Comment on the morphology of the red blood cells.
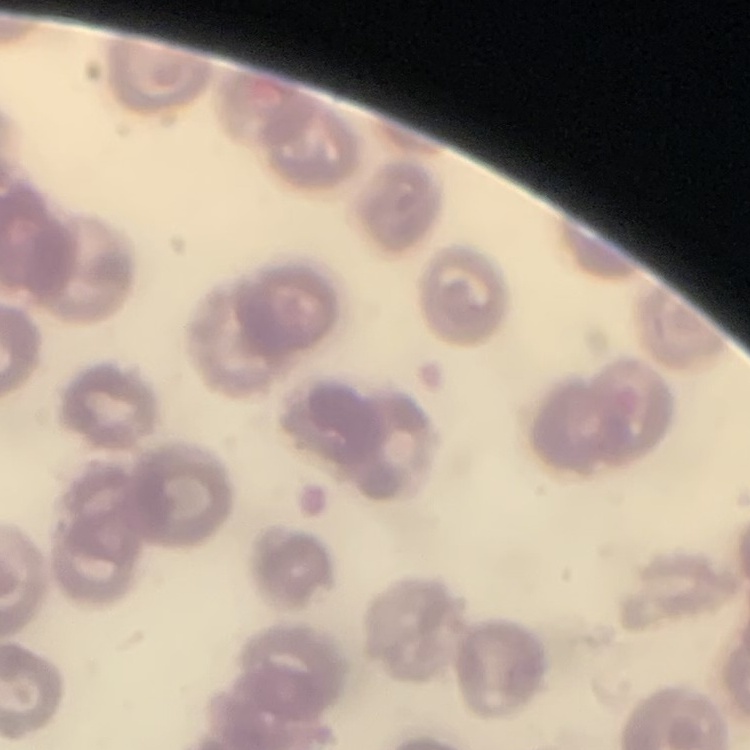

No rouleaux formation.

Summary:
  - Preparation: thin peripheral smear
  - Stain: Field's or Giemsa
  - Image type: square crop of a larger photomicrograph